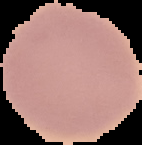
Summary:
  - Preparation: thin blood film
  - Image type: cell region segmented out of the field of view; surrounding area masked to black
  - Result: no malaria parasites detected
  - Image size: 142×145 pixels